Classify this cell by malaria status.
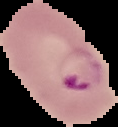
Parasitized.

image size = 118×127 pixels
image type = segmented cell region on a black background
preparation = thin blood smear